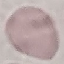

Result: no malaria parasites seen. Cell patch, automatically extracted from a larger field of view and resized to 64 × 64 pixels. Acquired by smartphone through the microscope eyepiece. Thin blood film. Giemsa-stained preparation.